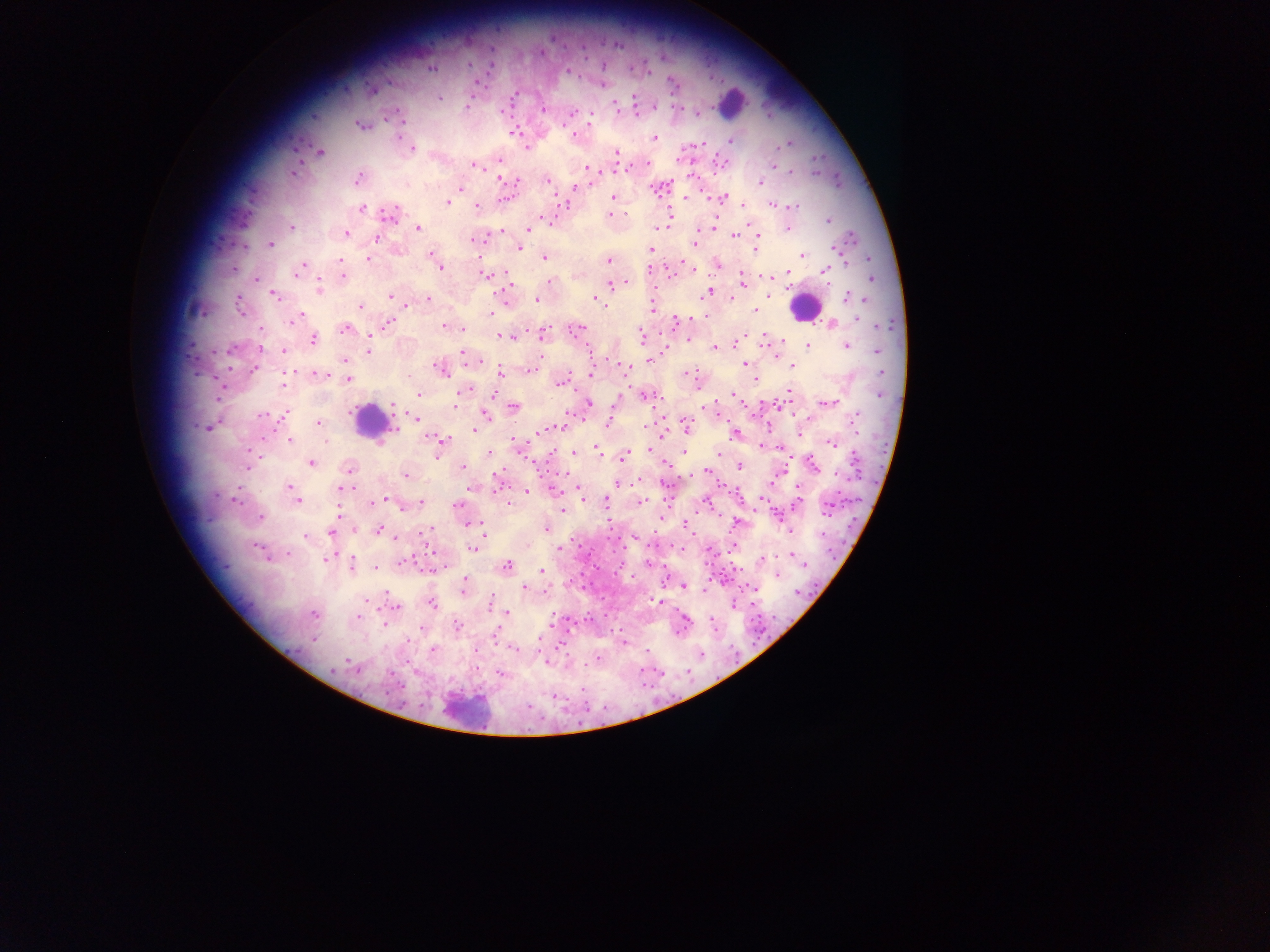
Approximate centers as (x, y) in pixels.
Summary:
  - Leukocyte locations: (730, 100), (804, 307), (370, 421), (469, 710)
  - Plasmodium parasite locations: (469, 63), (431, 69), (568, 71), (672, 82), (515, 94), (439, 98), (633, 99), (467, 106), (656, 106), (615, 107), (543, 110), (502, 111), (570, 114), (590, 124), (360, 126), (514, 132), (574, 135), (398, 137), (653, 137), (730, 140), (786, 144), (527, 148), (413, 149), (320, 152), (617, 152), (499, 159), (647, 163), (475, 166), (773, 167), (586, 168), (790, 171), (293, 173), (500, 176), (357, 179), (547, 180), (760, 182), (460, 187), (574, 187), (612, 197), (503, 198), (686, 198), (722, 198), (447, 202), (477, 206), (773, 206), (794, 207), (362, 208), (391, 214), (609, 215), (828, 220), (291, 227), (418, 228), (656, 228), (787, 228), (528, 229), (757, 232), (346, 233), (734, 235), (377, 238), (472, 240), (695, 241), (271, 244), (518, 247), (757, 248), (835, 248), (651, 250), (432, 254), (802, 255), (545, 257), (339, 259), (368, 259), (435, 260), (608, 261), (682, 263), (717, 264), (302, 265), (440, 267), (788, 272), (824, 272), (297, 273), (485, 275), (343, 276), (256, 279), (742, 279), (550, 282), (612, 284), (625, 284), (320, 287), (707, 292), (275, 295), (390, 295), (847, 297), (428, 298), (855, 298), (536, 300), (596, 300), (239, 305), (361, 306), (652, 309), (755, 311), (489, 315), (857, 319), (294, 320), (675, 320), (390, 323), (831, 323), (444, 326), (578, 328), (345, 329), (462, 329), (545, 333), (641, 335), (502, 337), (688, 338), (312, 339), (808, 345), (260, 346), (847, 346), (714, 347), (231, 349), (369, 350), (284, 351), (878, 351), (464, 353), (649, 360), (345, 361), (745, 363), (792, 366), (439, 368), (254, 370), (530, 370), (625, 370), (500, 372), (591, 373), (686, 373), (290, 374), (320, 374), (347, 379), (756, 379), (561, 382), (283, 385), (464, 390), (790, 392), (418, 394), (734, 394), (456, 397), (645, 397), (589, 403), (828, 403), (514, 406), (394, 407), (486, 414), (568, 414), (263, 415), (283, 416), (415, 417), (808, 418), (854, 420), (319, 422), (609, 422), (687, 422), (552, 427), (645, 427), (209, 428), (473, 429), (733, 433), (444, 439), (290, 442), (831, 444), (596, 449), (648, 449), (574, 452), (490, 453), (685, 453), (718, 453), (438, 455), (624, 458), (311, 462), (813, 465), (248, 466), (740, 466), (463, 467), (349, 470), (706, 471), (837, 474), (406, 475), (618, 484), (288, 487), (797, 488), (340, 489), (291, 492), (527, 492), (580, 493), (762, 496), (298, 500), (382, 500), (235, 501), (642, 501), (421, 502), (606, 502), (457, 506), (402, 507), (562, 510), (338, 514), (261, 517), (719, 517), (545, 528), (379, 530), (692, 531), (789, 531), (654, 532), (331, 533), (632, 534), (304, 537), (394, 538), (607, 538), (257, 547), (474, 548), (681, 548), (558, 549), (723, 552), (288, 554), (326, 558), (762, 560), (403, 563), (351, 564), (506, 566), (376, 569), (542, 570), (617, 571), (777, 575), (465, 581), (463, 586), (684, 586), (584, 587), (524, 588), (741, 588), (386, 593), (651, 599), (490, 603), (432, 604), (396, 607), (508, 613), (314, 614), (359, 617), (709, 617), (384, 624), (457, 627), (675, 631), (497, 632), (313, 639), (625, 639), (432, 649), (514, 649), (598, 654), (349, 661), (546, 663), (584, 663), (687, 666), (642, 668), (332, 669), (500, 673), (606, 706)
  - Image size: 1270×952 pixels
  - Preparation: thick blood film
  - Field of view: single
  - Country: Ghana
  - Capture: mobile-phone photograph through a microscope